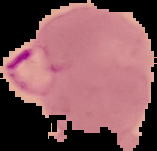

Summary:
  - Image type: segmented cell region on a black background
  - Malaria status: parasitized
  - Preparation: thin blood smear
  - Image size: 157×151 pixels